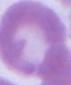

magnification = 1000x
modality = micrograph
identification = red blood cell